Locate every blood parasite and identify its species.
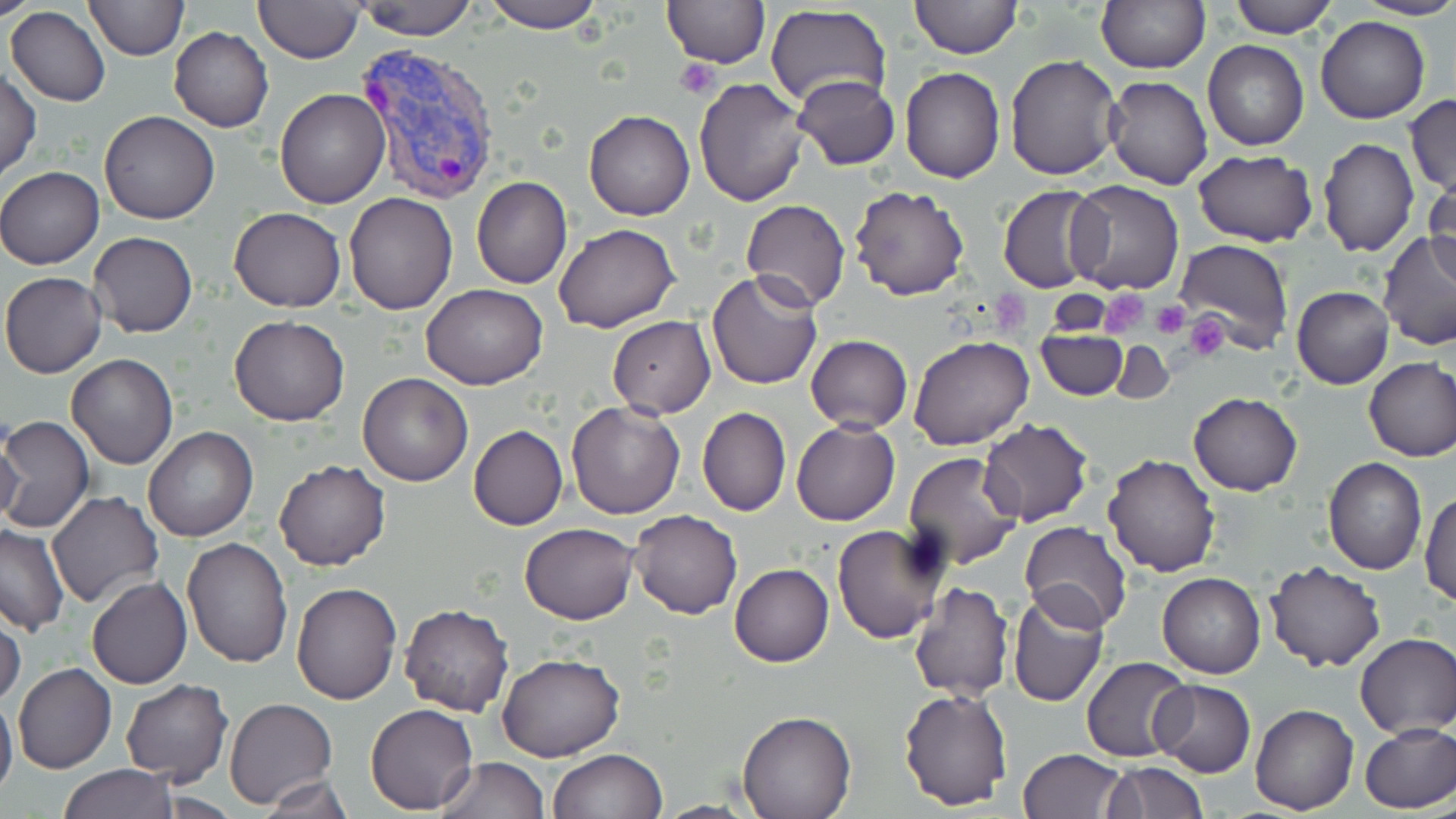
Approximate bounding boxes as named x1/y1/x2/y2 corners in pixels.
Plasmodium vivax-infected red blood cells: (x1=357, y1=43, x2=501, y2=203).
No Plasmodium falciparum, Plasmodium ovale, Plasmodium malariae, Babesia divergens, or Trypanosoma brucei observed.

slide-level diagnosis = Plasmodium vivax
magnification = 1000x
image size = 1456×819 pixels
preparation = thin blood smear
stain = May-Grünwald-Giemsa
field of view = one of a larger specimen
platelet locations = approximate bounding boxes as named x1/y1/x2/y2 corners in pixels: (x1=676, y1=58, x2=720, y2=99), (x1=994, y1=289, x2=1031, y2=331), (x1=1098, y1=289, x2=1150, y2=340), (x1=1150, y1=300, x2=1190, y2=341), (x1=1159, y1=304, x2=1214, y2=344), (x1=1185, y1=313, x2=1230, y2=360)
uninfected red blood cell locations = approximate bounding boxes as named x1/y1/x2/y2 corners in pixels: (x1=1, y1=0, x2=37, y2=20), (x1=84, y1=0, x2=189, y2=61), (x1=252, y1=0, x2=363, y2=63), (x1=353, y1=0, x2=477, y2=41), (x1=479, y1=0, x2=603, y2=33), (x1=660, y1=0, x2=770, y2=68), (x1=908, y1=0, x2=1022, y2=58), (x1=1095, y1=0, x2=1211, y2=74), (x1=1225, y1=0, x2=1341, y2=38), (x1=1353, y1=0, x2=1456, y2=20), (x1=765, y1=4, x2=893, y2=108), (x1=6, y1=7, x2=111, y2=107), (x1=1317, y1=16, x2=1430, y2=123), (x1=169, y1=26, x2=274, y2=131), (x1=1202, y1=38, x2=1309, y2=151), (x1=1004, y1=54, x2=1125, y2=180), (x1=899, y1=65, x2=1006, y2=183), (x1=0, y1=66, x2=40, y2=181), (x1=791, y1=74, x2=900, y2=171), (x1=694, y1=76, x2=809, y2=207), (x1=1105, y1=76, x2=1215, y2=190), (x1=275, y1=87, x2=390, y2=209), (x1=1405, y1=94, x2=1456, y2=196), (x1=99, y1=110, x2=219, y2=223), (x1=584, y1=110, x2=695, y2=221), (x1=1316, y1=137, x2=1420, y2=255), (x1=1192, y1=150, x2=1318, y2=246), (x1=0, y1=166, x2=104, y2=269), (x1=1425, y1=175, x2=1455, y2=286), (x1=471, y1=177, x2=573, y2=290), (x1=1064, y1=182, x2=1184, y2=295), (x1=849, y1=184, x2=970, y2=301), (x1=997, y1=185, x2=1109, y2=294), (x1=344, y1=192, x2=457, y2=314), (x1=741, y1=198, x2=850, y2=312), (x1=229, y1=207, x2=346, y2=311), (x1=553, y1=224, x2=681, y2=333), (x1=1377, y1=230, x2=1456, y2=353), (x1=89, y1=231, x2=198, y2=338), (x1=1176, y1=239, x2=1296, y2=352), (x1=707, y1=269, x2=823, y2=390), (x1=1, y1=272, x2=106, y2=378), (x1=420, y1=285, x2=548, y2=389), (x1=1293, y1=286, x2=1394, y2=390), (x1=227, y1=315, x2=350, y2=425), (x1=607, y1=315, x2=715, y2=418), (x1=1035, y1=329, x2=1128, y2=399), (x1=806, y1=335, x2=912, y2=433), (x1=908, y1=335, x2=1034, y2=450), (x1=1109, y1=340, x2=1174, y2=402), (x1=66, y1=354, x2=179, y2=471), (x1=1363, y1=358, x2=1456, y2=462), (x1=357, y1=372, x2=473, y2=486), (x1=1188, y1=391, x2=1302, y2=496), (x1=565, y1=401, x2=685, y2=519), (x1=696, y1=407, x2=791, y2=517), (x1=1, y1=415, x2=95, y2=533), (x1=977, y1=419, x2=1092, y2=528), (x1=791, y1=420, x2=900, y2=526), (x1=469, y1=425, x2=568, y2=531), (x1=0, y1=427, x2=28, y2=535), (x1=144, y1=427, x2=258, y2=542), (x1=901, y1=452, x2=1023, y2=572), (x1=1101, y1=453, x2=1219, y2=576), (x1=1323, y1=457, x2=1427, y2=574), (x1=274, y1=459, x2=390, y2=570), (x1=45, y1=490, x2=163, y2=611), (x1=1420, y1=491, x2=1455, y2=606), (x1=629, y1=509, x2=742, y2=619), (x1=1020, y1=520, x2=1131, y2=631), (x1=520, y1=522, x2=638, y2=624), (x1=0, y1=524, x2=69, y2=634), (x1=832, y1=524, x2=949, y2=644), (x1=182, y1=536, x2=293, y2=668), (x1=1266, y1=562, x2=1384, y2=672), (x1=729, y1=564, x2=834, y2=668), (x1=1157, y1=571, x2=1266, y2=678), (x1=86, y1=577, x2=193, y2=690), (x1=291, y1=581, x2=402, y2=705), (x1=907, y1=582, x2=1014, y2=701), (x1=1007, y1=590, x2=1111, y2=706), (x1=399, y1=604, x2=514, y2=716), (x1=0, y1=608, x2=26, y2=711), (x1=1354, y1=632, x2=1455, y2=738), (x1=497, y1=652, x2=624, y2=762), (x1=1082, y1=655, x2=1193, y2=762), (x1=13, y1=662, x2=117, y2=774), (x1=121, y1=679, x2=232, y2=785), (x1=1150, y1=679, x2=1256, y2=778), (x1=898, y1=686, x2=1014, y2=811), (x1=0, y1=695, x2=17, y2=802), (x1=224, y1=696, x2=338, y2=807), (x1=366, y1=703, x2=478, y2=814), (x1=1251, y1=704, x2=1359, y2=815), (x1=737, y1=711, x2=855, y2=819), (x1=1360, y1=722, x2=1456, y2=812), (x1=550, y1=748, x2=669, y2=819), (x1=1017, y1=749, x2=1128, y2=819), (x1=435, y1=756, x2=548, y2=819), (x1=1103, y1=762, x2=1208, y2=818), (x1=58, y1=763, x2=179, y2=819), (x1=256, y1=774, x2=354, y2=819)
modality = optical microscopy